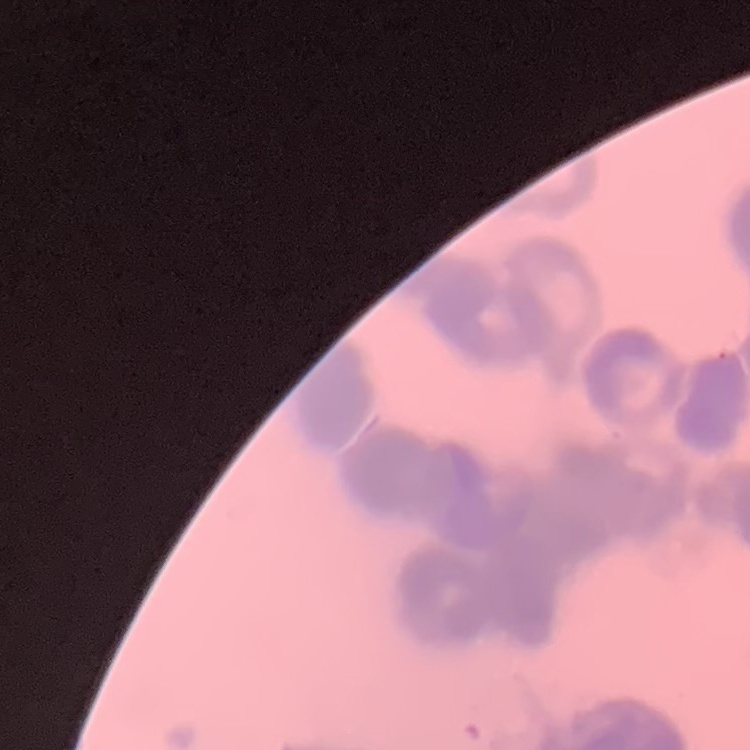 The erythrocytes exhibit rouleaux formation. One tile cut from a larger photomicrograph. Thin blood smear. Field's or Giemsa stain.